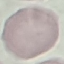

Malaria status: uninfected. Thin blood smear. Acquired by smartphone through the microscope eyepiece. Automatically extracted cell patch, resized to 64 × 64 pixels. Giemsa stain.